Report the malaria status of this cell.
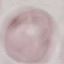
Uninfected.

Summary:
  - Preparation: thin blood smear
  - Image type: automatically extracted cell patch, resized to 64 × 64 pixels
  - Capture: smartphone camera at the microscope eyepiece
  - Stain: Giemsa